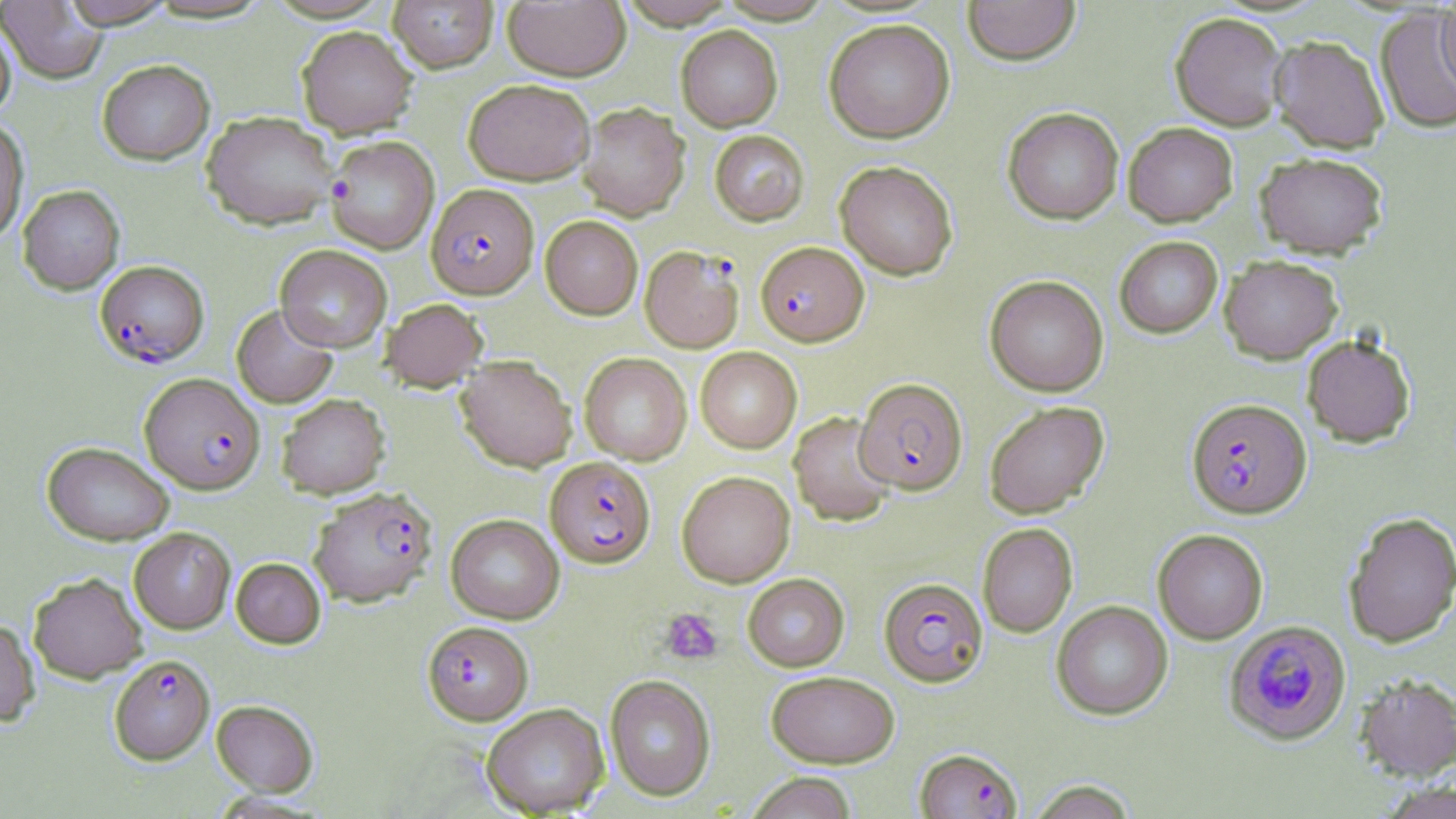
Summary:
  - Coordinate format: approximate bounding boxes as (x1, y1, x2, y2) in pixels
  - Platelet locations: (660, 607, 723, 664)
  - Uninfected red blood cell locations (subset): (60, 0, 177, 28), (387, 0, 498, 72), (616, 0, 739, 29), (962, 0, 1081, 65), (1, 1, 108, 85), (503, 1, 630, 81), (1436, 1, 1456, 94), (1374, 8, 1456, 134), (1170, 11, 1288, 130), (824, 18, 955, 143), (0, 19, 16, 120), (297, 25, 418, 138), (676, 25, 783, 131), (1269, 35, 1389, 152), (97, 59, 215, 165), (463, 78, 594, 185), (576, 102, 689, 220), (1003, 107, 1123, 224), (201, 110, 339, 230), (0, 118, 30, 244), (1123, 122, 1238, 227), (710, 130, 809, 226), (326, 136, 439, 253), (1254, 151, 1389, 258), (835, 160, 958, 280), (18, 185, 125, 294), (540, 215, 642, 319), (1114, 236, 1223, 338), (275, 244, 392, 351), (1219, 255, 1342, 363), (985, 275, 1109, 397), (381, 298, 488, 392), (232, 304, 338, 408), (1301, 333, 1416, 448), (695, 347, 802, 453), (579, 352, 692, 465), (455, 355, 576, 471), (277, 393, 390, 498), (984, 401, 1109, 518), (789, 412, 896, 526), (42, 441, 174, 545), (677, 470, 795, 587), (1343, 511, 1456, 648), (446, 514, 565, 623), (977, 523, 1077, 637), (128, 528, 235, 634), (1153, 529, 1268, 644), (231, 557, 326, 648), (28, 572, 147, 683), (743, 574, 849, 671), (1051, 600, 1172, 720), (0, 618, 40, 727), (766, 670, 901, 768), (1353, 673, 1456, 782), (605, 674, 715, 800), (211, 699, 319, 795), (481, 702, 609, 817), (744, 772, 858, 819), (1025, 780, 1139, 818), (1377, 781, 1456, 819)
  - Plasmodium falciparum-infected red blood cell locations (subset): (427, 183, 538, 298), (756, 241, 868, 346), (640, 245, 745, 352), (95, 260, 209, 367), (854, 378, 968, 494), (1187, 398, 1311, 518), (545, 456, 656, 567), (309, 487, 437, 607), (879, 577, 988, 686), (1223, 620, 1351, 746), (422, 621, 533, 725), (109, 654, 214, 764), (915, 747, 1021, 819)
  - Slide-level diagnosis: Plasmodium falciparum
  - Modality: optical microscopy
  - Stain: May-Grünwald-Giemsa
  - Image size: 1456×819 pixels
  - Field of view: one of a larger specimen
  - Preparation: thin blood film
  - Magnification: 1000x